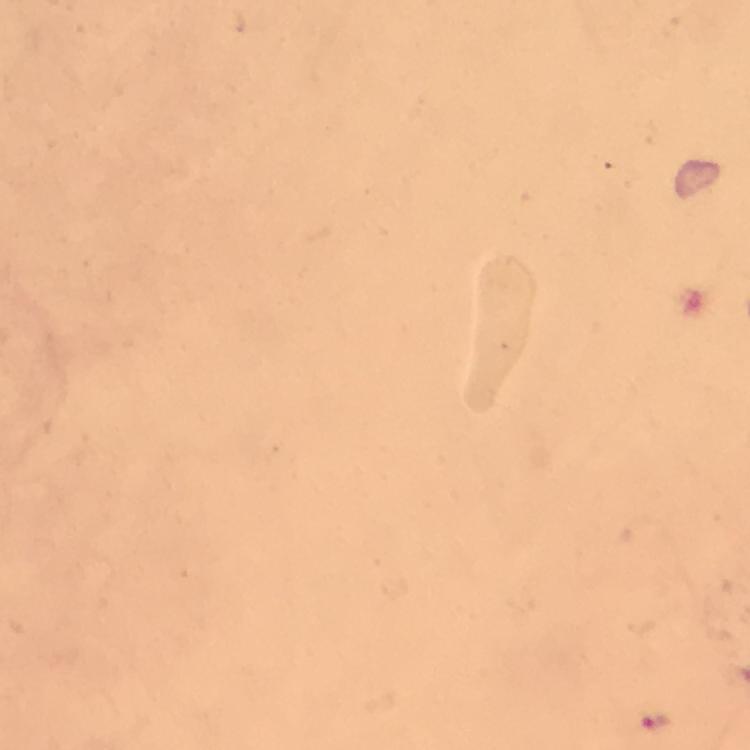

{
  "image_size": "750×750 pixels",
  "malaria_parasite_locations": "approximate centers as {x, y} in pixels: {654, 721}",
  "capture": "smartphone photograph through a microscope",
  "context": "from a diagnostic examination for malaria",
  "magnification": "100x",
  "cropped_from": "one field of view",
  "preparation": "thick blood film",
  "stain": "Giemsa",
  "immersion_oil": "used"
}